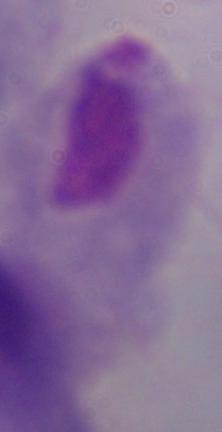
Summary:
  - Modality: photomicrograph
  - Magnification: 1000x
  - Identification: trichomonad